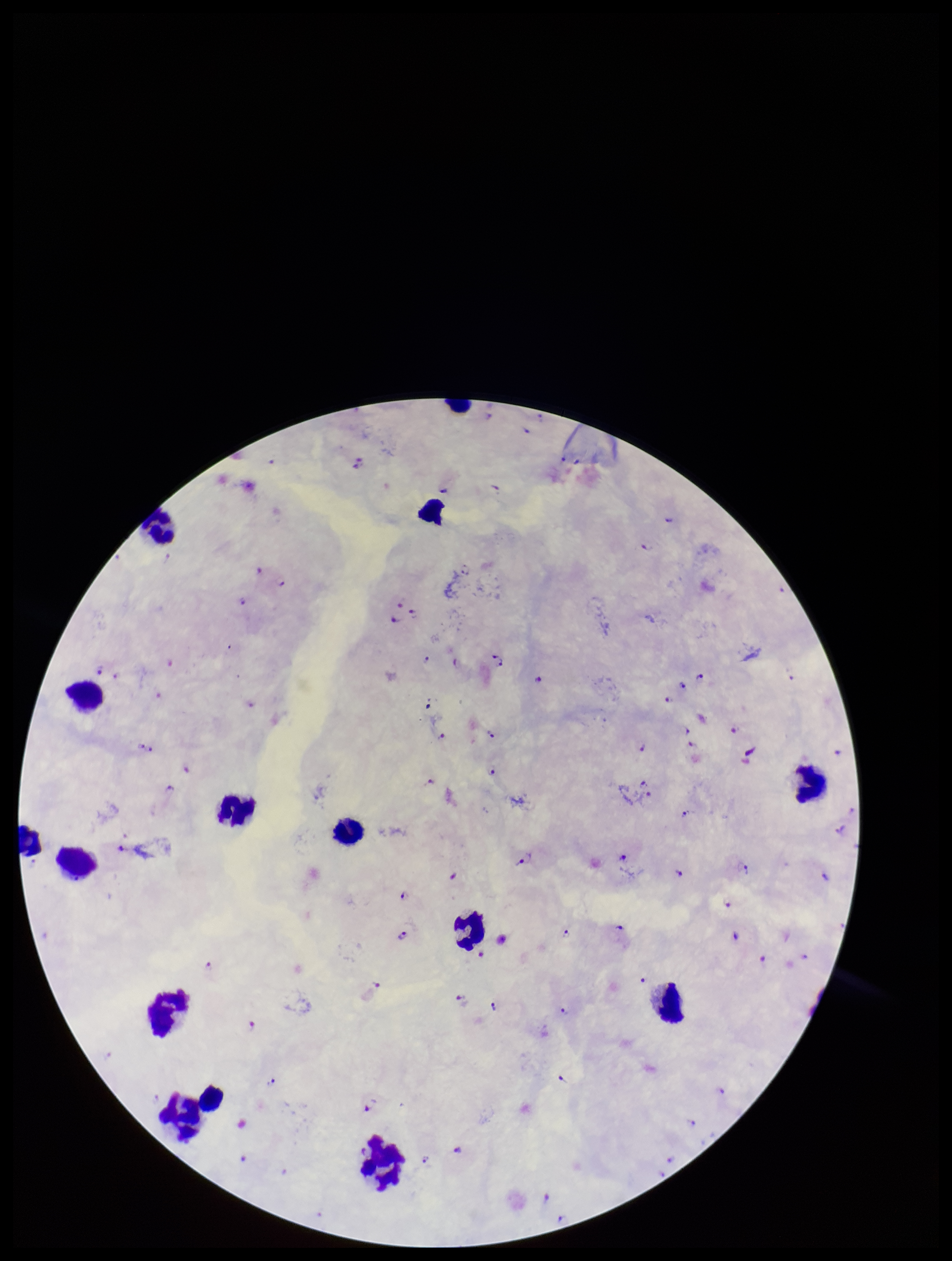 Patient malaria status: infected. Smartphone photograph taken through the eyepiece of a microscope. Plasmodium parasites: identified. Giemsa stain. Parasite count: 96. Image is 952×1261 pixels. Preparation: thick smear. Leukocyte count: 14. Species reported for this patient: Plasmodium falciparum. Single field of view.